Comment on the morphology of the erythrocytes.
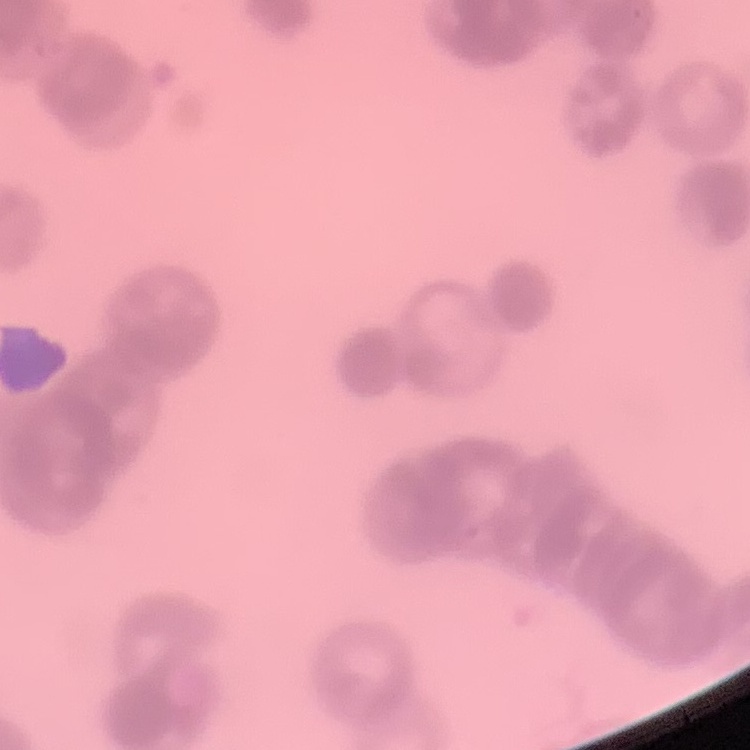

They show rouleaux formation.

Summary:
  - Preparation: thin blood film
  - Stain: Field's or Giemsa
  - Image type: square crop of a larger photomicrograph